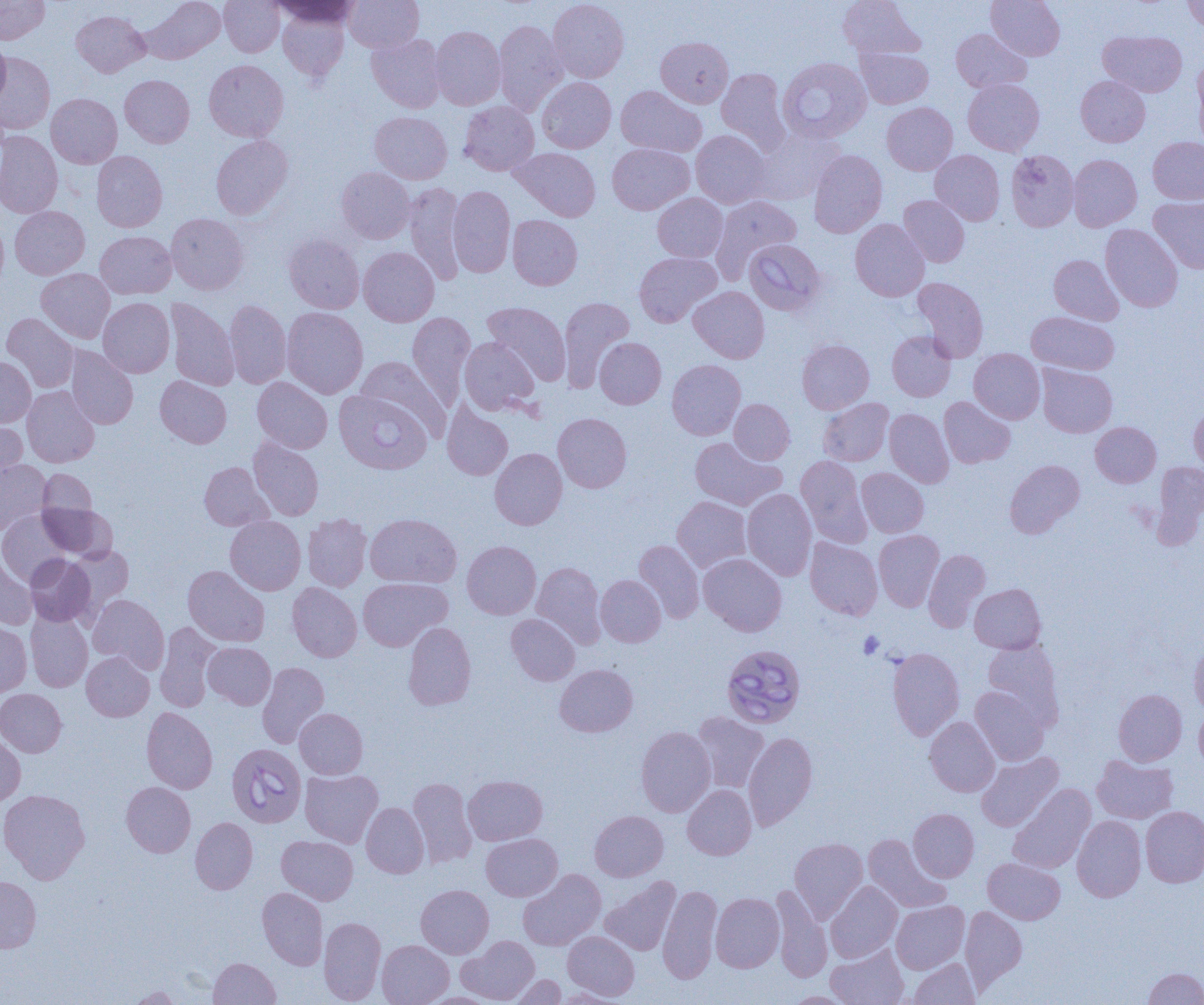
Summary:
  - Coordinate format: approximate bounding boxes as [x1, y1, x2, y2] in pixels
  - Platelet locations: [858, 631, 883, 659]
  - Uninfected red blood cell locations: [0, 0, 49, 45], [141, 0, 225, 64], [219, 0, 284, 57], [271, 0, 361, 27], [344, 0, 423, 52], [548, 0, 629, 82], [838, 0, 924, 61], [986, 0, 1065, 60], [1182, 0, 1204, 31], [278, 8, 350, 81], [71, 10, 149, 77], [494, 20, 567, 116], [430, 26, 506, 110], [951, 29, 1031, 93], [1099, 30, 1187, 97], [367, 33, 447, 112], [0, 35, 11, 109], [656, 36, 733, 108], [857, 46, 934, 109], [0, 52, 55, 135], [204, 59, 288, 142], [1192, 61, 1204, 145], [716, 68, 789, 151], [120, 75, 194, 147], [1076, 75, 1150, 147], [537, 77, 616, 153], [963, 78, 1044, 156], [615, 85, 707, 157], [46, 93, 122, 168], [459, 101, 539, 175], [882, 102, 957, 175], [370, 111, 452, 184], [750, 129, 842, 205], [691, 130, 772, 208], [0, 131, 63, 218], [211, 135, 293, 219], [1148, 136, 1204, 204], [607, 143, 694, 214], [510, 147, 601, 221], [808, 150, 887, 238], [930, 150, 1004, 225], [1006, 150, 1079, 232], [91, 151, 167, 232], [1068, 154, 1142, 231], [336, 167, 415, 243], [405, 183, 466, 283], [448, 186, 515, 277], [653, 193, 728, 262], [710, 194, 802, 281], [899, 195, 969, 267], [1149, 196, 1204, 274], [10, 206, 90, 279], [166, 212, 249, 295], [507, 215, 582, 290], [0, 217, 9, 295], [850, 219, 929, 301], [1100, 224, 1183, 312], [95, 231, 176, 299], [283, 233, 364, 313], [359, 246, 439, 326], [634, 251, 721, 327], [1049, 254, 1123, 325], [36, 268, 115, 343], [912, 277, 989, 362], [689, 286, 770, 363], [98, 297, 174, 377], [558, 297, 634, 391], [165, 299, 239, 390], [224, 300, 292, 389], [483, 302, 571, 385], [282, 307, 368, 398], [407, 311, 475, 407], [1026, 311, 1119, 374], [1, 313, 79, 392], [887, 331, 956, 402], [459, 337, 539, 415], [595, 337, 666, 409], [797, 339, 874, 413], [65, 347, 138, 430], [969, 349, 1045, 424], [356, 356, 449, 439], [0, 357, 36, 427], [667, 360, 746, 440], [1037, 364, 1117, 437], [155, 375, 231, 448], [252, 376, 332, 453], [21, 386, 99, 468], [939, 396, 1015, 468], [818, 398, 893, 466], [729, 399, 794, 464], [442, 402, 513, 480], [1189, 402, 1204, 474], [884, 408, 953, 488], [553, 413, 632, 493], [0, 418, 27, 484], [1090, 421, 1161, 487], [248, 436, 324, 521], [690, 437, 785, 510], [490, 448, 567, 530], [796, 456, 872, 547], [0, 459, 51, 534], [1004, 459, 1085, 538], [199, 461, 273, 530], [1151, 461, 1204, 548], [856, 467, 929, 538], [38, 469, 97, 522], [742, 488, 816, 580], [672, 496, 752, 572], [38, 502, 116, 561], [0, 510, 72, 585], [365, 513, 461, 588], [302, 514, 372, 591], [225, 516, 306, 595], [873, 530, 944, 611], [805, 537, 882, 620], [633, 539, 704, 623], [462, 541, 541, 619], [65, 546, 134, 619], [923, 549, 990, 631], [699, 553, 787, 636], [25, 554, 96, 627], [0, 556, 36, 630], [532, 562, 606, 649], [183, 565, 269, 647], [596, 575, 666, 647], [358, 578, 452, 651], [287, 582, 362, 662], [969, 583, 1046, 654], [88, 594, 169, 673], [25, 609, 93, 692], [506, 614, 580, 685], [0, 621, 31, 698], [403, 621, 476, 710], [154, 622, 221, 712], [981, 639, 1064, 729], [203, 642, 276, 709], [1189, 643, 1204, 717], [887, 647, 964, 740], [81, 652, 154, 721], [257, 662, 329, 748], [554, 664, 638, 737], [970, 686, 1049, 766], [0, 689, 67, 756], [1113, 689, 1187, 765], [141, 707, 218, 794], [1194, 707, 1204, 774], [295, 708, 367, 779], [691, 712, 769, 792], [924, 716, 999, 796], [636, 726, 716, 817], [743, 731, 818, 830], [0, 733, 25, 806], [976, 752, 1063, 831], [1092, 754, 1178, 823], [300, 769, 383, 847], [463, 775, 547, 845], [408, 778, 477, 867], [121, 782, 195, 857], [1007, 784, 1096, 874], [682, 785, 756, 859], [0, 789, 90, 883], [361, 802, 429, 878], [1140, 806, 1204, 887], [908, 808, 979, 882], [590, 810, 668, 881], [1072, 815, 1146, 902], [190, 817, 257, 894], [481, 833, 562, 901], [863, 834, 950, 912], [277, 835, 358, 905], [789, 838, 867, 921], [983, 858, 1065, 924], [518, 869, 606, 951], [0, 876, 41, 953], [600, 876, 681, 956], [825, 881, 903, 963], [416, 884, 494, 958], [658, 884, 722, 984], [770, 886, 832, 982], [257, 887, 328, 970], [711, 893, 784, 972], [891, 900, 969, 974], [960, 906, 1027, 991], [318, 917, 386, 1004], [563, 931, 639, 1000], [457, 935, 539, 1004], [377, 940, 454, 1005], [825, 944, 909, 1005], [209, 957, 281, 1004], [909, 958, 980, 1004], [1143, 967, 1204, 1004], [507, 974, 566, 1004], [126, 986, 183, 1004], [553, 988, 627, 1004], [781, 991, 857, 1004], [418, 992, 502, 1005]
  - Babesia divergens-infected red blood cell locations: [777, 57, 871, 143], [743, 239, 826, 316], [334, 389, 431, 475], [721, 644, 806, 728], [227, 743, 306, 827]
  - Slide-level diagnosis: Babesia divergens
  - Modality: optical microscopy
  - Preparation: thin blood film
  - Magnification: 1000x
  - Field of view: single
  - Image size: 1204×1005 pixels